Identify the cell.
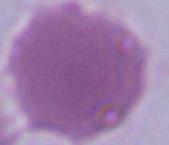

An erythrocyte.

Summary:
  - Modality: micrograph
  - Magnification: 1000x